Classify this cell by malaria status.
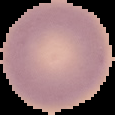

It is uninfected.

The area outside the segmented cell region is set to black. From a thin blood film. Image is 115×115 pixels.